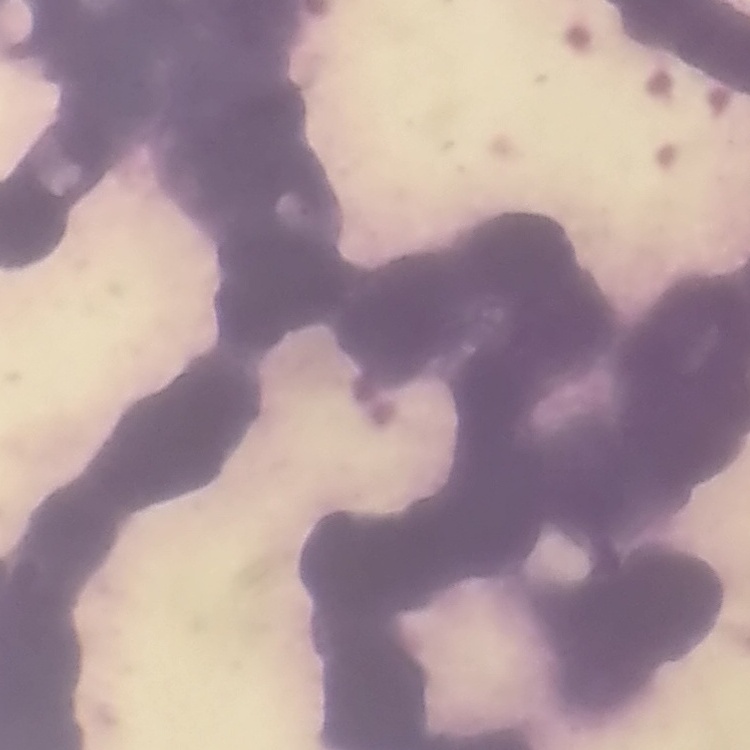
The erythrocytes show rouleaux formation. Field's or Giemsa stain. Thin blood film. One tile cut from a larger photomicrograph.